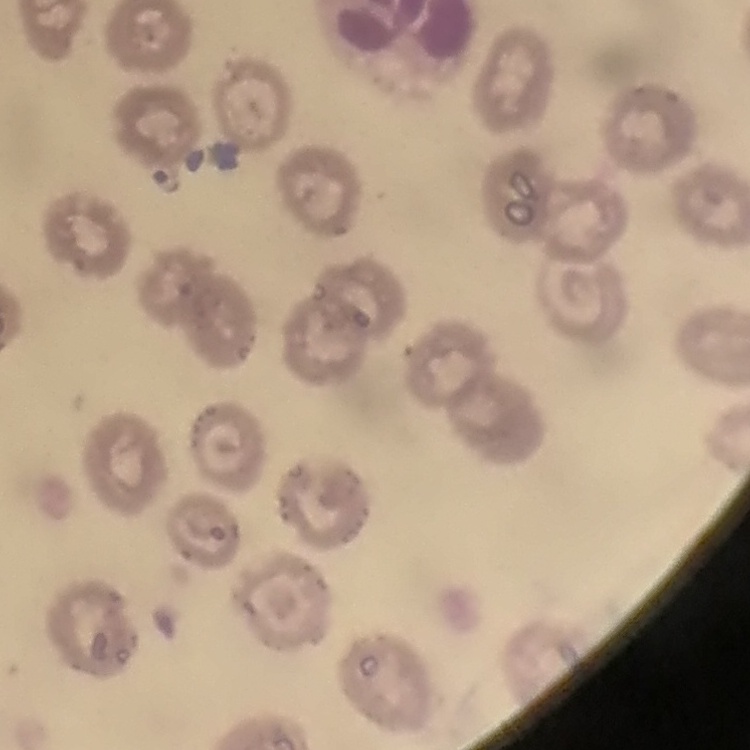

The erythrocytes exhibit no rouleaux formation. Square crop of a larger photomicrograph. Field's or Giemsa stain. Thin blood film.